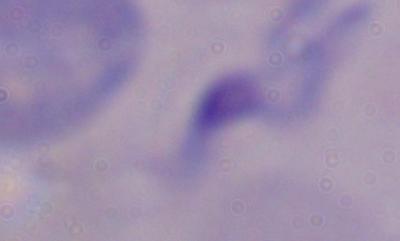
Summary:
  - Magnification: 1000x
  - Modality: micrograph
  - Identification: trypanosome